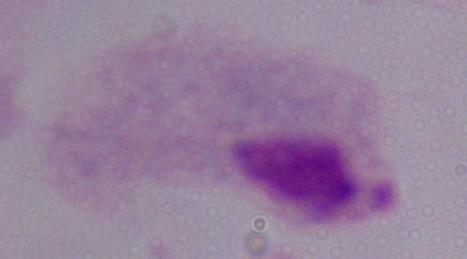

modality = micrograph
identification = trichomonad
magnification = 1000x